Report the malaria status of this cell.
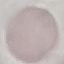
Uninfected.

{
  "preparation": "thin smear",
  "stain": "Giemsa",
  "image_type": "cell patch, automatically extracted from a larger field of view and resized to 64 × 64 pixels",
  "capture": "smartphone camera at the microscope eyepiece"
}